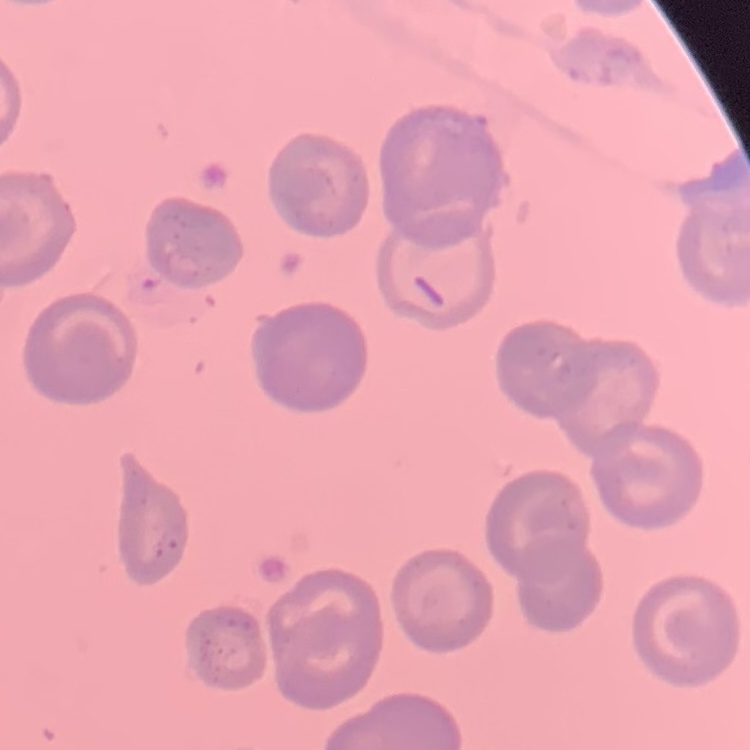

erythrocyte morphology = no rouleaux formation
preparation = thin blood film
image type = one tile cut from a larger photomicrograph
stain = Field's or Giemsa